Classify this cell by malaria status.
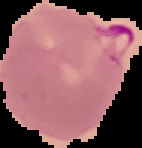

Parasitized.

The area outside the segmented cell region is set to black. Image is 142×148 pixels. From a thin blood film.